Locate platelets.
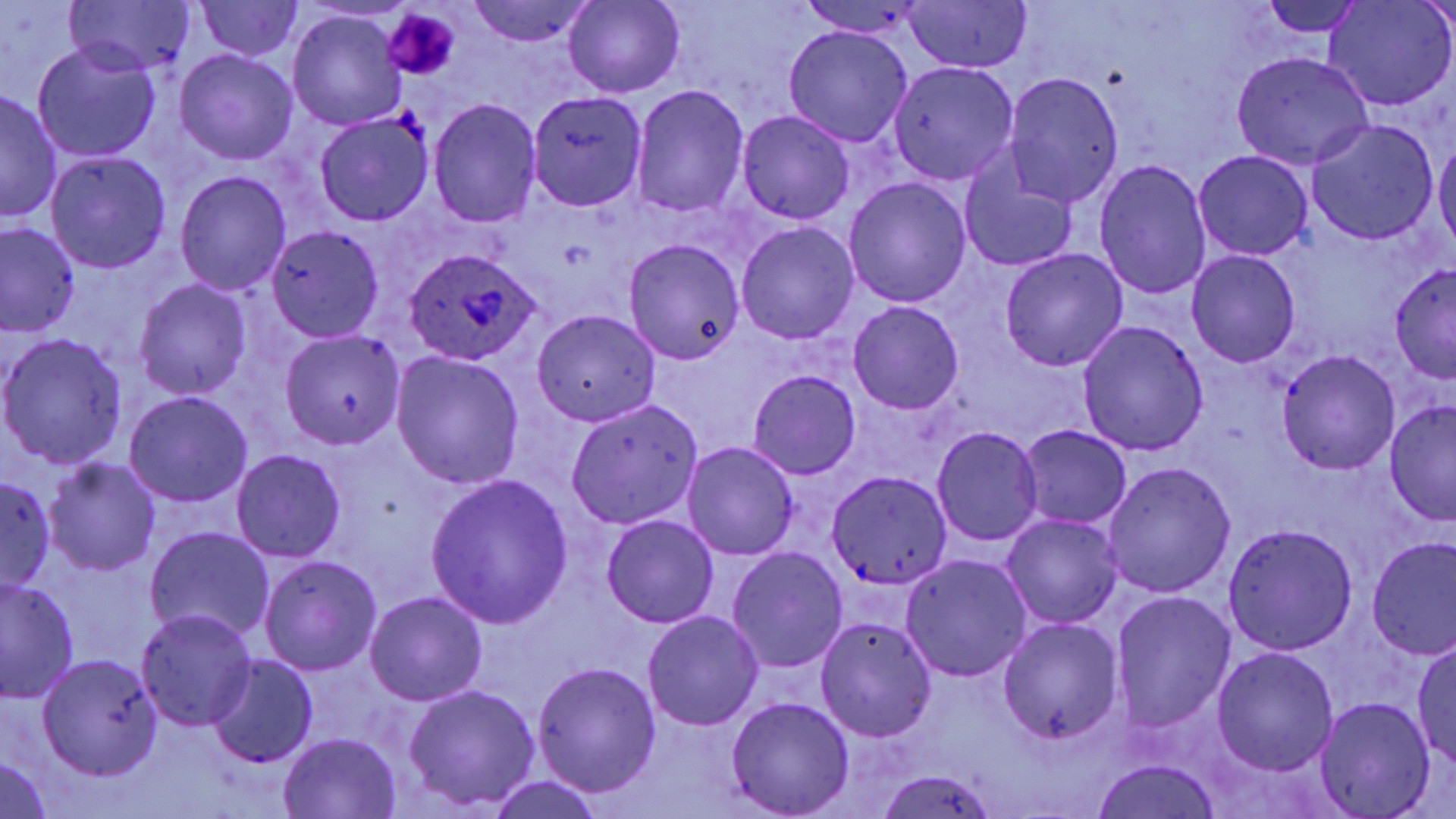
Approximate bounding boxes as named x1/y1/x2/y2 corners in pixels.
Platelets: (x1=384, y1=10, x2=457, y2=79).

Uninfected red blood cell locations: (x1=65, y1=0, x2=194, y2=75), (x1=563, y1=0, x2=683, y2=97), (x1=904, y1=0, x2=1030, y2=73), (x1=197, y1=1, x2=304, y2=61), (x1=467, y1=1, x2=594, y2=47), (x1=801, y1=1, x2=928, y2=39), (x1=1256, y1=1, x2=1372, y2=37), (x1=1322, y1=1, x2=1454, y2=111), (x1=288, y1=11, x2=408, y2=129), (x1=782, y1=26, x2=913, y2=147), (x1=33, y1=41, x2=162, y2=163), (x1=175, y1=49, x2=297, y2=164), (x1=1231, y1=52, x2=1374, y2=169), (x1=888, y1=61, x2=1019, y2=185), (x1=1004, y1=71, x2=1125, y2=210), (x1=632, y1=85, x2=750, y2=218), (x1=0, y1=90, x2=61, y2=223), (x1=526, y1=91, x2=648, y2=212), (x1=428, y1=98, x2=542, y2=228), (x1=737, y1=109, x2=855, y2=225), (x1=315, y1=113, x2=434, y2=226), (x1=1306, y1=119, x2=1438, y2=245), (x1=1434, y1=138, x2=1456, y2=251), (x1=1192, y1=150, x2=1314, y2=261), (x1=46, y1=152, x2=172, y2=274), (x1=960, y1=153, x2=1079, y2=273), (x1=1093, y1=159, x2=1212, y2=300), (x1=174, y1=170, x2=291, y2=295), (x1=844, y1=177, x2=971, y2=307), (x1=736, y1=222, x2=858, y2=344), (x1=1, y1=223, x2=79, y2=336), (x1=266, y1=225, x2=385, y2=341), (x1=624, y1=238, x2=746, y2=364), (x1=999, y1=249, x2=1127, y2=371), (x1=1186, y1=250, x2=1301, y2=368), (x1=1390, y1=262, x2=1456, y2=382), (x1=134, y1=279, x2=251, y2=400), (x1=848, y1=301, x2=964, y2=416), (x1=531, y1=309, x2=662, y2=426), (x1=1076, y1=320, x2=1209, y2=456), (x1=281, y1=328, x2=406, y2=450), (x1=1, y1=333, x2=129, y2=469), (x1=1277, y1=350, x2=1400, y2=474), (x1=391, y1=351, x2=525, y2=489), (x1=748, y1=369, x2=861, y2=478), (x1=125, y1=390, x2=253, y2=507), (x1=1383, y1=398, x2=1456, y2=524), (x1=564, y1=399, x2=702, y2=528), (x1=1017, y1=425, x2=1133, y2=529), (x1=932, y1=426, x2=1044, y2=545), (x1=682, y1=442, x2=800, y2=560), (x1=232, y1=450, x2=345, y2=563), (x1=44, y1=459, x2=161, y2=575), (x1=1102, y1=462, x2=1235, y2=598), (x1=827, y1=470, x2=952, y2=592), (x1=0, y1=472, x2=54, y2=594), (x1=426, y1=475, x2=573, y2=629), (x1=1002, y1=514, x2=1124, y2=628), (x1=601, y1=515, x2=718, y2=629), (x1=1223, y1=523, x2=1358, y2=655), (x1=144, y1=526, x2=276, y2=645), (x1=1366, y1=537, x2=1456, y2=660), (x1=727, y1=547, x2=849, y2=674), (x1=902, y1=554, x2=1033, y2=681), (x1=260, y1=555, x2=382, y2=676), (x1=1, y1=576, x2=79, y2=704), (x1=1112, y1=591, x2=1238, y2=736), (x1=366, y1=592, x2=489, y2=707), (x1=135, y1=609, x2=258, y2=733), (x1=643, y1=611, x2=762, y2=731), (x1=815, y1=617, x2=937, y2=741), (x1=997, y1=618, x2=1124, y2=746), (x1=1412, y1=641, x2=1455, y2=769), (x1=1212, y1=646, x2=1338, y2=774), (x1=34, y1=655, x2=163, y2=781), (x1=208, y1=655, x2=317, y2=767), (x1=532, y1=662, x2=661, y2=797), (x1=403, y1=684, x2=540, y2=810), (x1=724, y1=696, x2=856, y2=818), (x1=1316, y1=697, x2=1436, y2=818), (x1=279, y1=733, x2=400, y2=818), (x1=0, y1=756, x2=53, y2=818), (x1=1089, y1=758, x2=1220, y2=819), (x1=873, y1=767, x2=1001, y2=819), (x1=488, y1=775, x2=605, y2=819). Plasmodium ovale-infected red blood cell locations: (x1=408, y1=251, x2=542, y2=364). Slide-level diagnosis: Plasmodium ovale. Optical microscopy. 1000x magnification. Image is 1456×819 pixels. Single field of view. Thin blood smear. May-Grünwald-Giemsa stain.